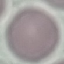
Summary:
  - Malaria status: uninfected
  - Capture: smartphone through the microscope eyepiece
  - Image type: automatically extracted cell patch, resized to 64 × 64 pixels
  - Preparation: thin blood smear
  - Stain: Giemsa